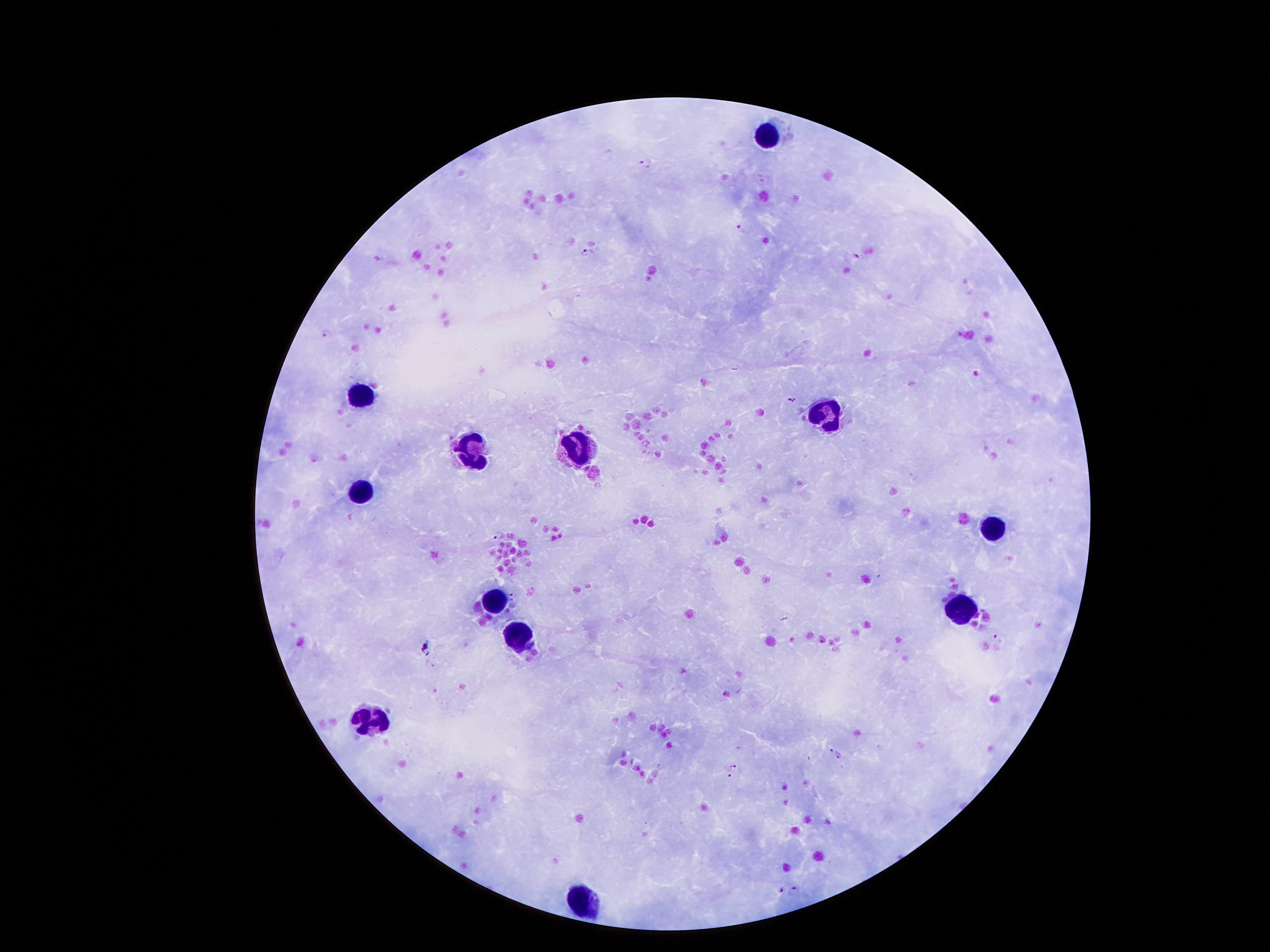

Approximate centers as (x, y) in pixels.
Summary:
  - Leukocyte locations: (773, 136), (357, 392), (821, 411), (470, 449), (582, 449), (361, 487), (993, 526), (493, 600), (962, 609), (521, 636), (370, 718), (580, 900)
  - Malaria parasite locations: (645, 164), (742, 226), (588, 252), (855, 257), (327, 332), (792, 400), (499, 535), (513, 597), (997, 638), (831, 751), (838, 755), (734, 767), (728, 775), (780, 890), (795, 892)
  - Preparation: thick blood film
  - Stain: Giemsa
  - Field of view: one from this slide
  - Magnification: 100x
  - Capture: smartphone through the microscope eyepiece
  - Patient malaria status: infected with Plasmodium falciparum
  - Image size: 1270×952 pixels